Point out Plasmodium parasites and leukocytes.
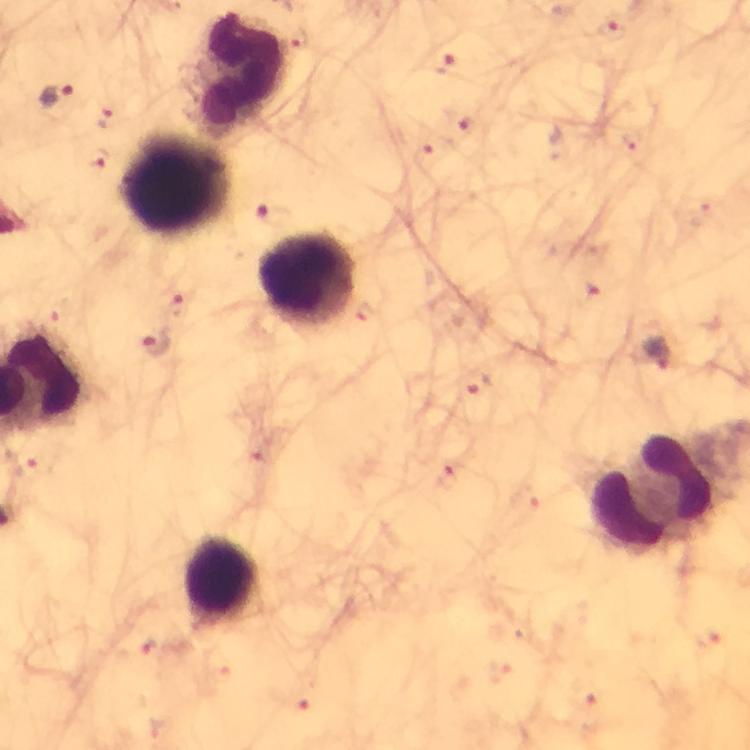

Approximate centers as {x, y} in pixels.
Plasmodium parasites: {611, 32}, {293, 42}, {446, 65}, {54, 97}, {463, 127}, {426, 156}, {273, 213}, {588, 291}, {179, 307}, {158, 342}, {656, 352}, {477, 384}, {261, 452}, {446, 475}, {706, 637}, {150, 649}, {302, 702}, {594, 711}.
Leukocytes: {238, 76}, {175, 183}, {306, 278}, {653, 493}, {220, 582}.

Summary:
  - Context: from a diagnostic examination for malaria
  - Capture: smartphone mounted on the microscope
  - Immersion oil: used
  - Stain: Giemsa
  - Preparation: thick blood smear
  - Magnification: 100x
  - Image size: 750×750 pixels
  - Cropped from: one field of view